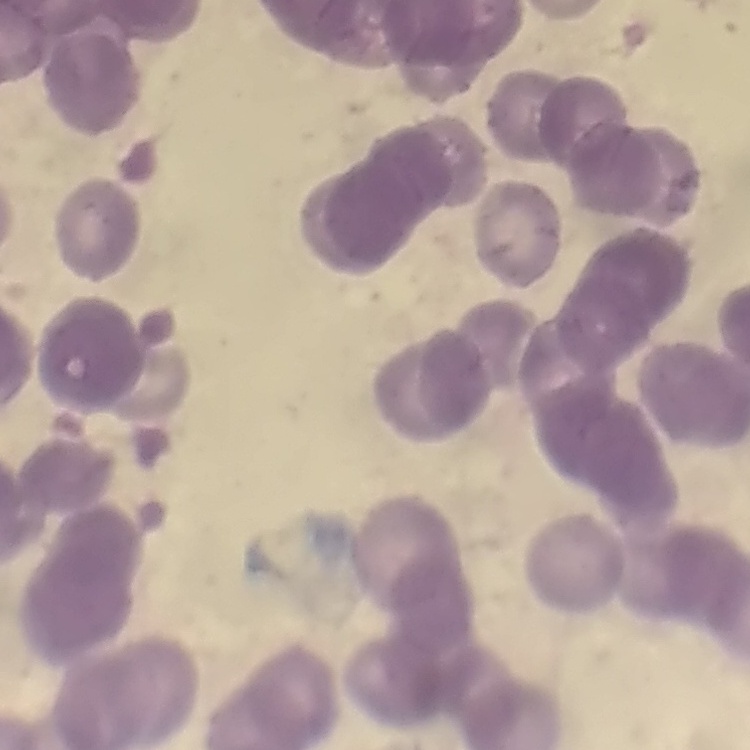

The erythrocytes exhibit rouleaux formation. Thin blood smear. Field's or Giemsa stain. One tile cut from a larger photomicrograph.